Name the parasite shown.
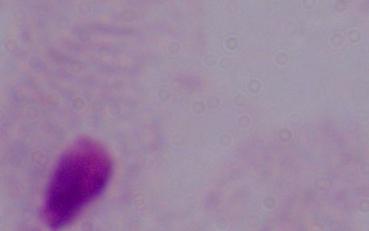
This is a trichomonad.

Summary:
  - Magnification: 1000x
  - Modality: photomicrograph